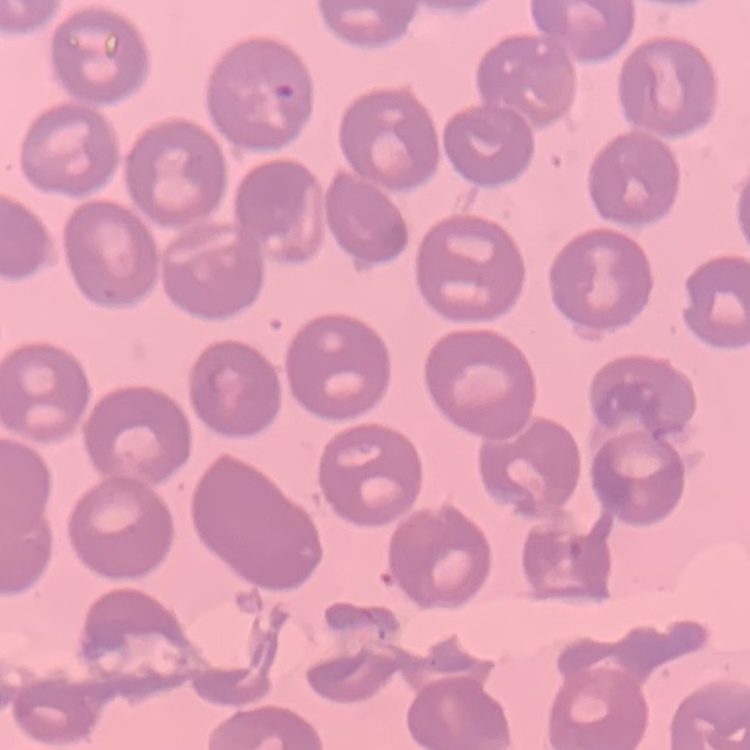 The erythrocytes show no rouleaux formation. Thin blood smear. Field's or Giemsa stain. Square crop of a larger photomicrograph.